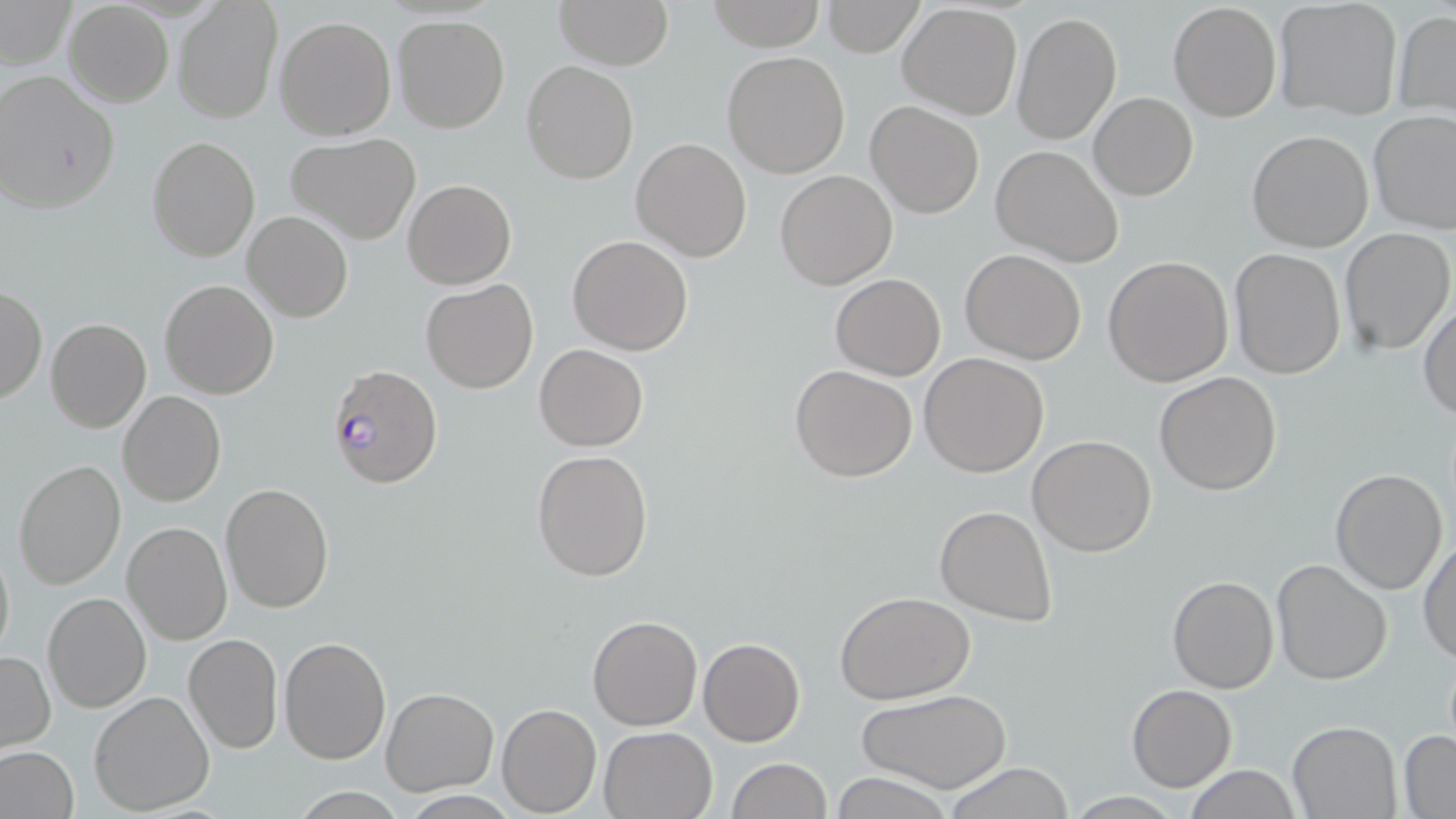

slide_level_diagnosis: Plasmodium falciparum
uninfected_red_blood_cell_locations: 'approximate bounding boxes as (x1,y1)-(x2,y2) corner pairs in pixels: (555,0)-(672,69), (707,0)-(824,51), (0,1)-(75,70), (1274,1)-(1402,118), (63,2)-(174,107), (172,2)-(281,123), (822,2)-(925,57), (1169,2)-(1282,121), (898,4)-(1023,120), (1391,9)-(1456,114), (1012,11)-(1121,144), (275,15)-(396,139), (394,15)-(509,133), (722,50)-(851,177), (521,59)-(638,184), (0,70)-(120,215), (1089,92)-(1197,200), (866,101)-(983,218), (1367,110)-(1456,235), (1247,129)-(1373,251), (287,132)-(421,243), (147,135)-(261,261), (630,137)-(752,261), (990,144)-(1124,267), (774,169)-(898,291), (403,179)-(515,289), (242,211)-(353,324), (1339,227)-(1455,356), (567,235)-(694,355), (960,248)-(1087,364), (1228,249)-(1346,378), (1103,255)-(1234,388), (831,273)-(945,380), (420,278)-(538,394), (159,279)-(279,400), (1,285)-(46,406), (1418,301)-(1455,420), (45,318)-(152,434), (534,343)-(648,450), (919,352)-(1050,477), (790,364)-(918,481), (1154,371)-(1282,496), (118,391)-(227,508), (1027,435)-(1157,557), (531,448)-(655,581), (12,459)-(125,589), (1329,467)-(1448,595), (220,483)-(335,614), (935,503)-(1057,626), (121,520)-(232,646), (1419,537)-(1456,666), (0,539)-(14,664), (1271,558)-(1394,685), (1167,574)-(1279,693), (834,590)-(976,704), (43,591)-(150,713), (587,613)-(702,731), (184,633)-(283,754), (280,635)-(392,764), (698,638)-(805,747), (1,651)-(55,751), (1126,684)-(1237,790), (381,686)-(499,795), (859,689)-(1011,793), (88,690)-(217,813), (497,702)-(602,816), (1286,721)-(1401,817), (599,725)-(719,818), (1397,730)-(1456,816), (0,746)-(81,819), (725,757)-(831,819), (942,762)-(1079,818), (1183,766)-(1303,819), (829,772)-(958,819)'
stain: May-Grünwald-Giemsa
field_of_view: single
plasmodium_falciparum_infected_red_blood_cell_locations: 'approximate bounding boxes as (x1,y1)-(x2,y2) corner pairs in pixels: (327,363)-(444,490)'
image_size: 1456×819 pixels
preparation: thin blood film
magnification: 1000x
modality: light microscopy